Assess the morphology of the red blood cells.
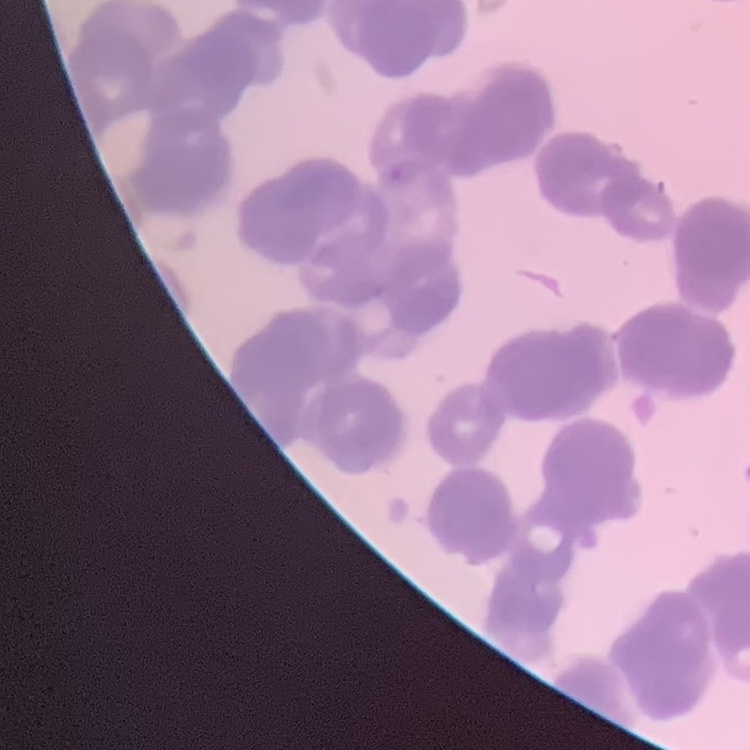

Rouleaux formation.

preparation: thin peripheral smear
stain: Field's or Giemsa
image_type: one tile cut from a larger photomicrograph